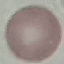 Malaria status: uninfected. Thin blood film. Acquired by smartphone through the microscope eyepiece. Giemsa stain. Cell patch, automatically extracted from a larger field of view and resized to 64 × 64 pixels.